Comment on the morphology of the red blood cells.
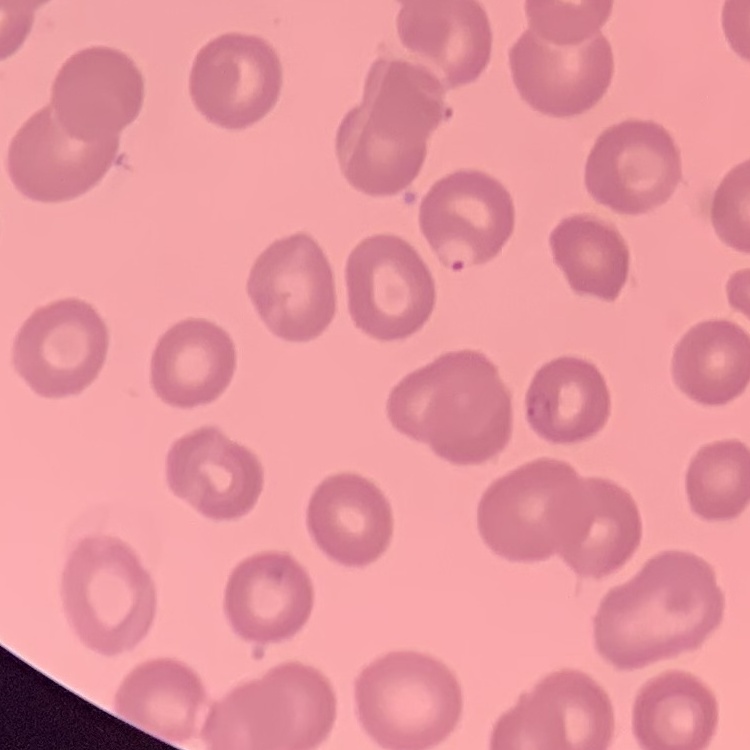

No rouleaux formation.

Summary:
  - Preparation: thin blood film
  - Image type: one tile cut from a larger photomicrograph
  - Stain: Field's or Giemsa